State which parasite is depicted.
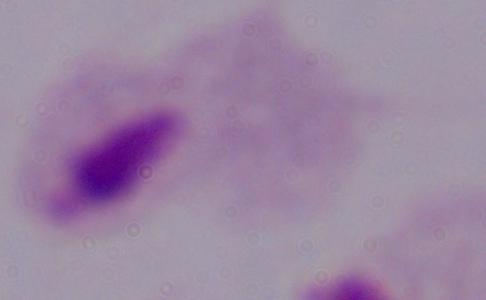
This is a trichomonad.

Photomicrograph. 1000x magnification.